Locate platelets.
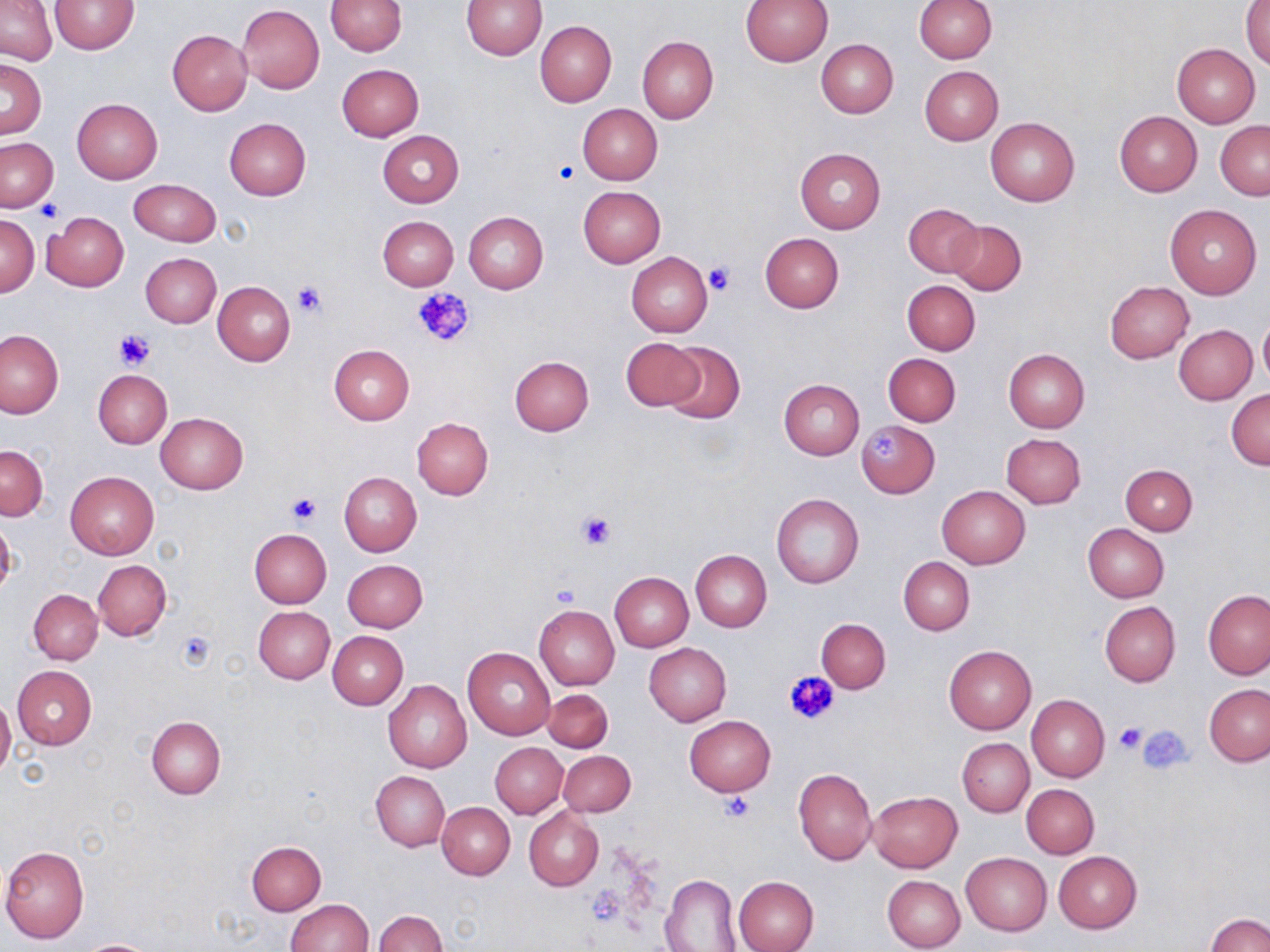

Approximate bounding boxes as [x1, y1, x2, y2] in pixels.
Platelets: [555, 158, 580, 185], [37, 199, 64, 223], [702, 263, 736, 297], [292, 282, 325, 317], [414, 286, 474, 348], [115, 330, 152, 369], [870, 433, 902, 464], [287, 492, 321, 526], [577, 510, 617, 550], [552, 582, 582, 608], [175, 630, 214, 669], [785, 669, 840, 725], [1114, 722, 1147, 755], [1137, 726, 1193, 774], [720, 792, 753, 821].

slide-level diagnosis = no evidence of blood parasites
modality = optical microscopy
field of view = single
uninfected red blood cell locations = approximate bounding boxes as [x1, y1, x2, y2] in pixels: [1, 0, 57, 65], [326, 0, 407, 56], [740, 0, 834, 65], [913, 0, 996, 62], [49, 1, 139, 54], [461, 1, 546, 59], [1243, 2, 1270, 69], [238, 4, 325, 94], [536, 21, 616, 106], [167, 29, 252, 115], [637, 36, 719, 123], [816, 39, 898, 117], [1172, 43, 1260, 127], [0, 59, 46, 137], [337, 64, 425, 141], [919, 66, 1004, 144], [72, 97, 162, 183], [578, 103, 663, 184], [1114, 111, 1203, 197], [986, 116, 1080, 206], [224, 117, 311, 199], [1216, 121, 1270, 199], [377, 130, 464, 207], [1, 138, 58, 211], [794, 148, 886, 233], [128, 179, 222, 246], [578, 186, 666, 266], [903, 203, 982, 278], [1165, 204, 1262, 299], [43, 211, 129, 291], [463, 211, 548, 293], [0, 214, 40, 297], [377, 215, 458, 289], [946, 219, 1026, 295], [760, 232, 844, 313], [140, 252, 221, 327], [627, 252, 713, 337], [902, 280, 981, 354], [213, 281, 295, 366], [1104, 281, 1193, 363], [1258, 317, 1270, 387], [1174, 325, 1257, 404], [0, 330, 65, 419], [621, 338, 706, 412], [661, 341, 746, 424], [328, 344, 414, 424], [1003, 349, 1090, 433], [884, 353, 961, 427], [509, 355, 594, 436], [92, 369, 171, 448], [779, 379, 864, 459], [1227, 388, 1270, 469], [156, 412, 248, 494], [412, 417, 493, 500], [857, 421, 939, 498], [1001, 434, 1086, 508], [0, 445, 48, 520], [1120, 464, 1197, 535], [65, 470, 159, 560], [339, 471, 421, 556], [937, 486, 1030, 569], [772, 493, 864, 590], [0, 514, 16, 600], [1083, 524, 1169, 602], [249, 528, 331, 607], [691, 550, 772, 631], [899, 557, 974, 635], [342, 559, 428, 633], [93, 560, 171, 640], [610, 572, 694, 652], [29, 589, 103, 665], [1203, 589, 1270, 679], [1099, 601, 1180, 687], [534, 604, 619, 690], [253, 606, 335, 683], [817, 618, 890, 693], [328, 630, 409, 709], [644, 642, 731, 725], [944, 645, 1035, 733], [463, 648, 556, 739], [12, 665, 97, 750], [383, 680, 472, 773], [1204, 684, 1270, 766], [544, 687, 613, 751], [1027, 694, 1110, 782], [0, 696, 16, 778], [684, 715, 776, 796], [146, 717, 225, 797], [958, 738, 1033, 816], [490, 743, 568, 818], [558, 749, 636, 817], [793, 767, 877, 865], [371, 772, 449, 851], [1022, 784, 1099, 857], [868, 790, 963, 873], [437, 802, 515, 879], [524, 807, 604, 890], [246, 841, 326, 915], [0, 844, 90, 943], [1053, 851, 1141, 933], [961, 853, 1051, 934], [881, 867, 1044, 945], [660, 873, 741, 951], [882, 875, 967, 951], [734, 876, 818, 952], [285, 898, 373, 951], [374, 909, 446, 952], [1206, 913, 1270, 952], [76, 939, 160, 952]
stain = May-Grünwald-Giemsa
preparation = thin blood smear
magnification = 1000x
image size = 1270×952 pixels